Name the parasite shown.
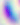
This is Toxoplasma gondii.

Captured at 400x magnification. Micrograph.